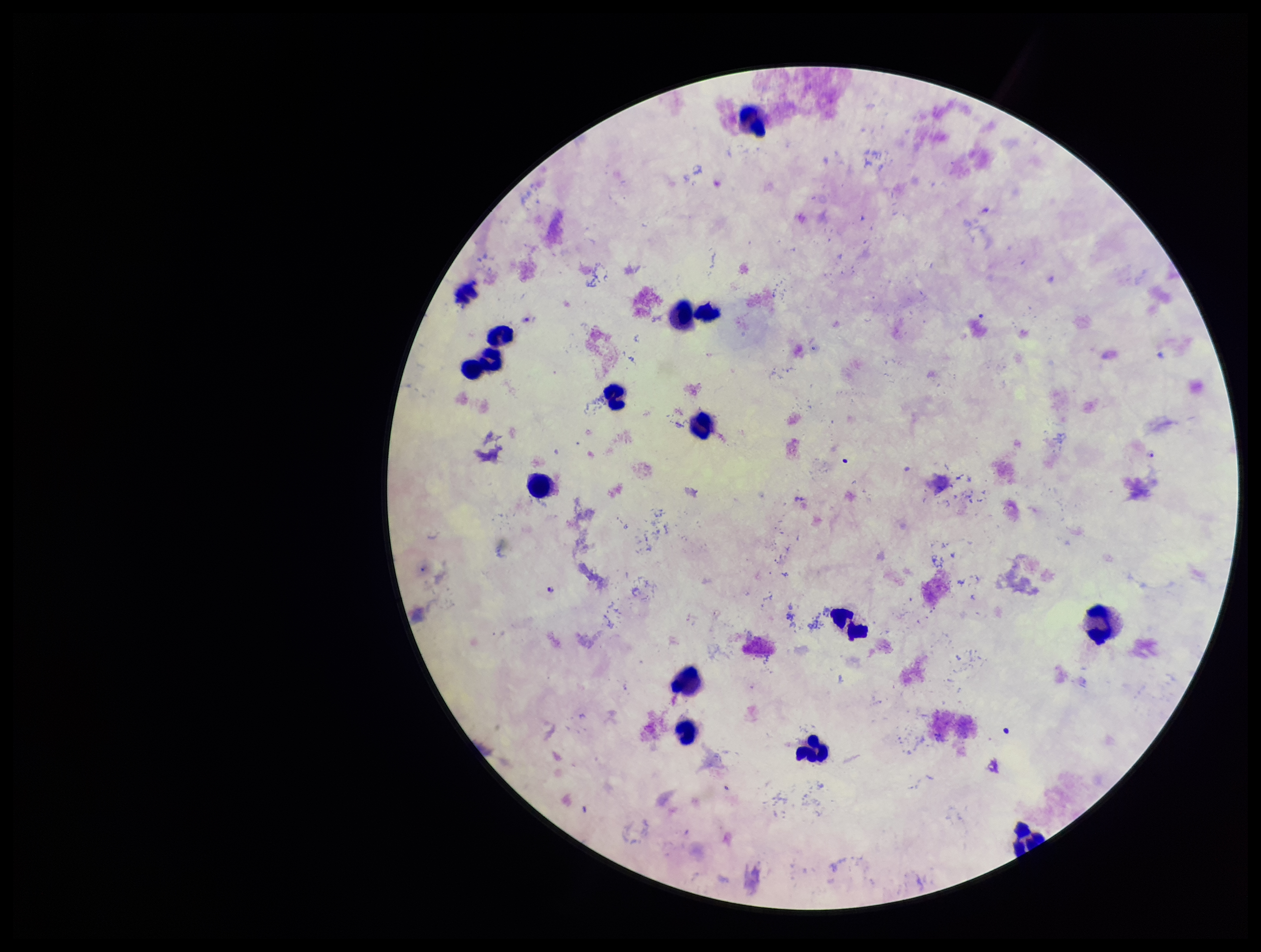

Summary:
  - Preparation: thick
  - Leukocyte count: 16
  - Image size: 1261×952 pixels
  - Capture: smartphone photograph through the microscope eyepiece
  - Patient malaria status: infected
  - Stain: Giemsa
  - Plasmodium parasites: identified
  - Field of view: single
  - Parasite count: 2
  - Species reported for this patient: Plasmodium falciparum